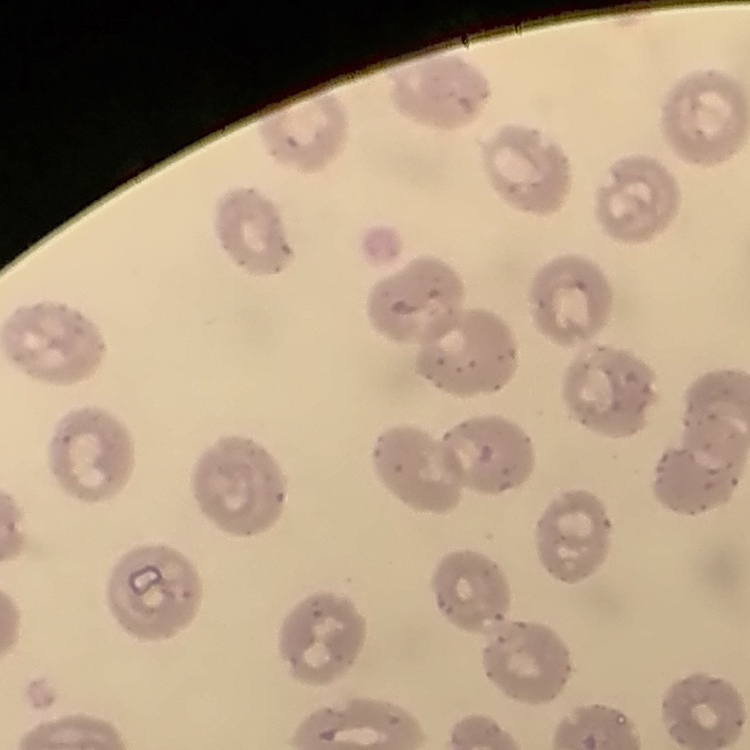

Summary:
  - Erythrocyte morphology: no rouleaux formation
  - Image type: one tile cut from a larger photomicrograph
  - Preparation: thin peripheral smear
  - Stain: Field's or Giemsa